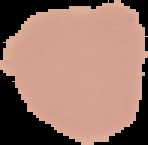

Summary:
  - Malaria status: uninfected
  - Preparation: thin blood smear
  - Image size: 148×145 pixels
  - Image type: cell region segmented out of the field of view; surrounding area masked to black